Identify the parasite.
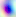

This is Toxoplasma gondii.

Summary:
  - Modality: micrograph
  - Magnification: 400x